Locate and identify every blood parasite.
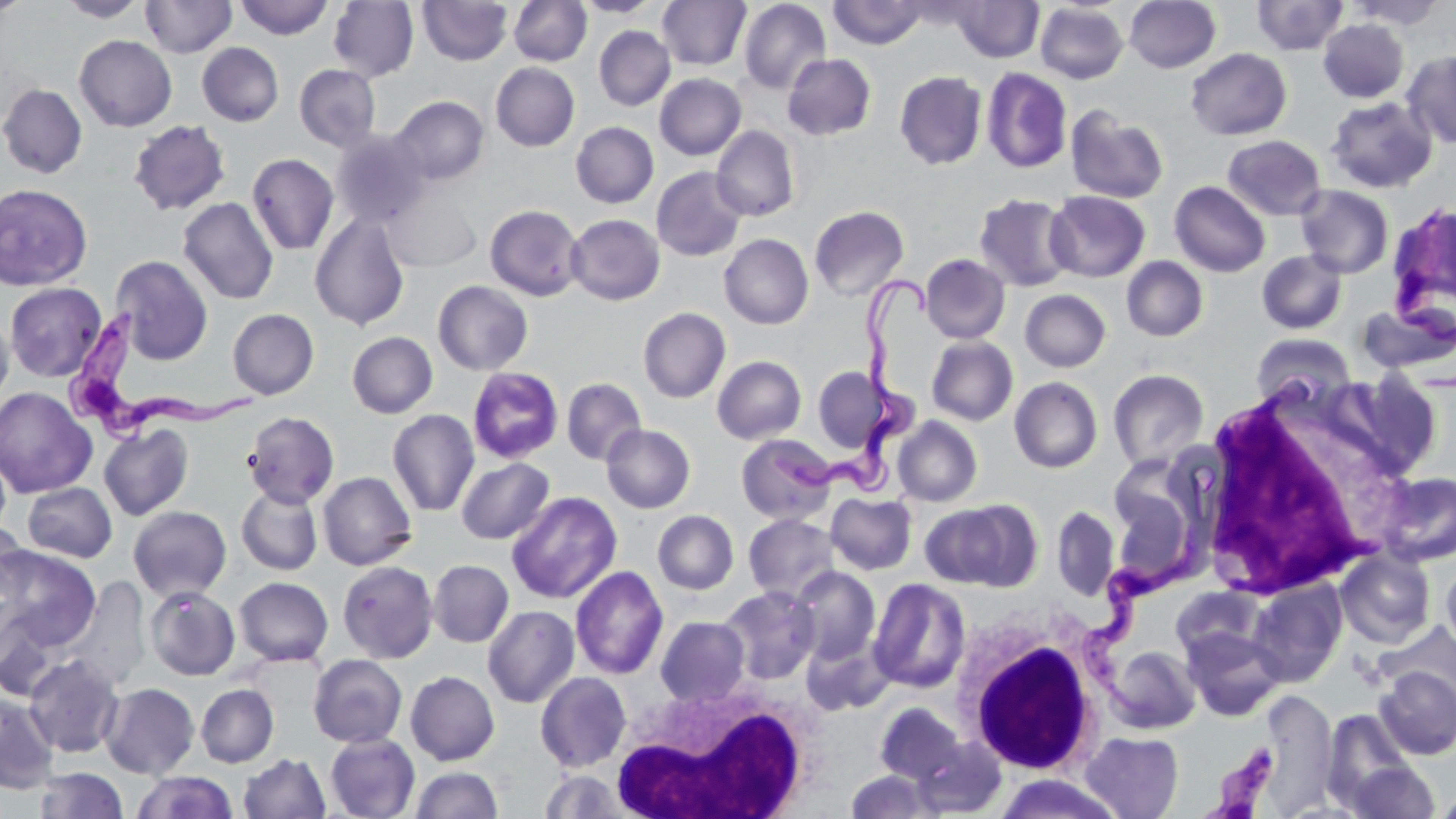

Approximate bounding boxes as (x1, y1, x2, y2) in pixels.
Trypanosoma brucei: (1390, 212, 1456, 349), (767, 275, 938, 502), (64, 309, 263, 444), (1083, 505, 1211, 727), (1200, 743, 1280, 819).
No Plasmodium falciparum, Plasmodium ovale, Plasmodium malariae, Plasmodium vivax, or Babesia divergens observed.

Summary:
  - White blood cell locations: (1196, 399, 1379, 601), (950, 606, 1107, 775), (610, 679, 817, 819)
  - Uninfected red blood cell locations: (1, 0, 32, 17), (57, 0, 149, 22), (140, 0, 237, 58), (236, 0, 333, 40), (418, 0, 512, 65), (509, 0, 591, 66), (574, 0, 661, 17), (657, 0, 751, 70), (829, 0, 928, 48), (952, 0, 1043, 62), (1125, 0, 1221, 73), (1252, 0, 1349, 55), (1347, 0, 1448, 29), (328, 1, 419, 82), (738, 1, 831, 95), (1036, 3, 1129, 84), (1318, 19, 1408, 103), (594, 26, 675, 110), (74, 35, 177, 132), (197, 43, 284, 126), (1185, 48, 1291, 141), (1403, 51, 1456, 149), (782, 53, 876, 140), (491, 62, 580, 151), (294, 64, 381, 151), (982, 67, 1072, 174), (894, 71, 987, 170), (655, 74, 746, 160), (0, 83, 88, 179), (391, 96, 488, 185), (1326, 96, 1438, 193), (1066, 106, 1169, 204), (127, 120, 230, 216), (571, 122, 658, 208), (711, 124, 800, 221), (331, 129, 430, 228), (1222, 135, 1326, 221), (247, 153, 339, 255), (652, 167, 748, 261), (1169, 181, 1270, 277), (0, 184, 93, 291), (1295, 185, 1394, 278), (1045, 190, 1150, 282), (384, 192, 481, 272), (973, 193, 1076, 292), (178, 197, 278, 304), (1387, 201, 1456, 318), (485, 205, 585, 301), (809, 205, 909, 301), (310, 213, 410, 331), (566, 214, 665, 305), (719, 233, 813, 329), (1256, 250, 1347, 335), (920, 254, 1011, 344), (111, 255, 213, 365), (1121, 256, 1208, 341), (433, 280, 533, 375), (4, 282, 107, 382), (1020, 289, 1111, 372), (1356, 304, 1455, 380), (638, 307, 730, 403), (227, 308, 319, 399), (0, 311, 14, 406), (347, 331, 437, 418), (1251, 333, 1356, 408), (927, 336, 1018, 425), (712, 356, 807, 444), (813, 366, 887, 452), (467, 367, 564, 464), (1108, 369, 1209, 472), (1319, 371, 1444, 483), (1010, 377, 1103, 473), (562, 378, 646, 466), (0, 387, 97, 498), (1194, 397, 1395, 600), (387, 409, 479, 517), (242, 411, 340, 507), (892, 416, 982, 507), (99, 423, 194, 521), (601, 424, 696, 513), (736, 434, 837, 525), (1108, 455, 1209, 582), (456, 457, 554, 544), (318, 471, 417, 570), (1375, 471, 1456, 567), (22, 482, 117, 562), (236, 484, 323, 575), (506, 491, 622, 604), (826, 493, 917, 574), (922, 501, 1039, 590), (128, 506, 231, 601), (1052, 506, 1119, 601), (653, 510, 739, 594), (744, 513, 839, 603), (0, 519, 28, 611), (0, 545, 100, 652), (1335, 549, 1436, 649), (1441, 555, 1456, 659), (428, 560, 514, 647), (337, 561, 438, 662), (570, 565, 668, 680), (789, 566, 880, 664), (59, 576, 151, 693), (234, 577, 333, 666), (868, 578, 970, 693), (1247, 580, 1347, 687), (719, 585, 821, 684), (145, 586, 241, 681), (1171, 586, 1264, 662), (0, 604, 69, 702), (483, 605, 580, 708), (656, 616, 750, 705), (1376, 623, 1456, 709), (1181, 626, 1285, 721), (801, 633, 893, 716), (1104, 645, 1201, 734), (308, 654, 407, 748), (24, 655, 124, 757), (1374, 666, 1456, 759), (405, 671, 500, 765), (535, 671, 632, 771), (1338, 680, 1443, 798), (100, 683, 199, 778), (196, 684, 279, 767), (1266, 692, 1342, 819), (0, 693, 59, 794), (874, 703, 966, 786), (1321, 710, 1415, 810), (1081, 731, 1184, 819), (325, 733, 420, 819), (912, 733, 1007, 816), (238, 753, 330, 818), (1346, 761, 1438, 819), (411, 766, 503, 817), (34, 767, 128, 819), (538, 769, 631, 818), (846, 769, 938, 818), (132, 772, 238, 819), (991, 773, 1123, 818), (1434, 789, 1456, 818)
  - Slide-level diagnosis: Trypanosoma brucei
  - Preparation: thin blood film
  - Field of view: one of a larger specimen
  - Magnification: 1000x
  - Modality: optical microscopy
  - Image size: 1456×819 pixels
  - Stain: May-Grünwald-Giemsa